Locate every leukocyte (white blood cell).
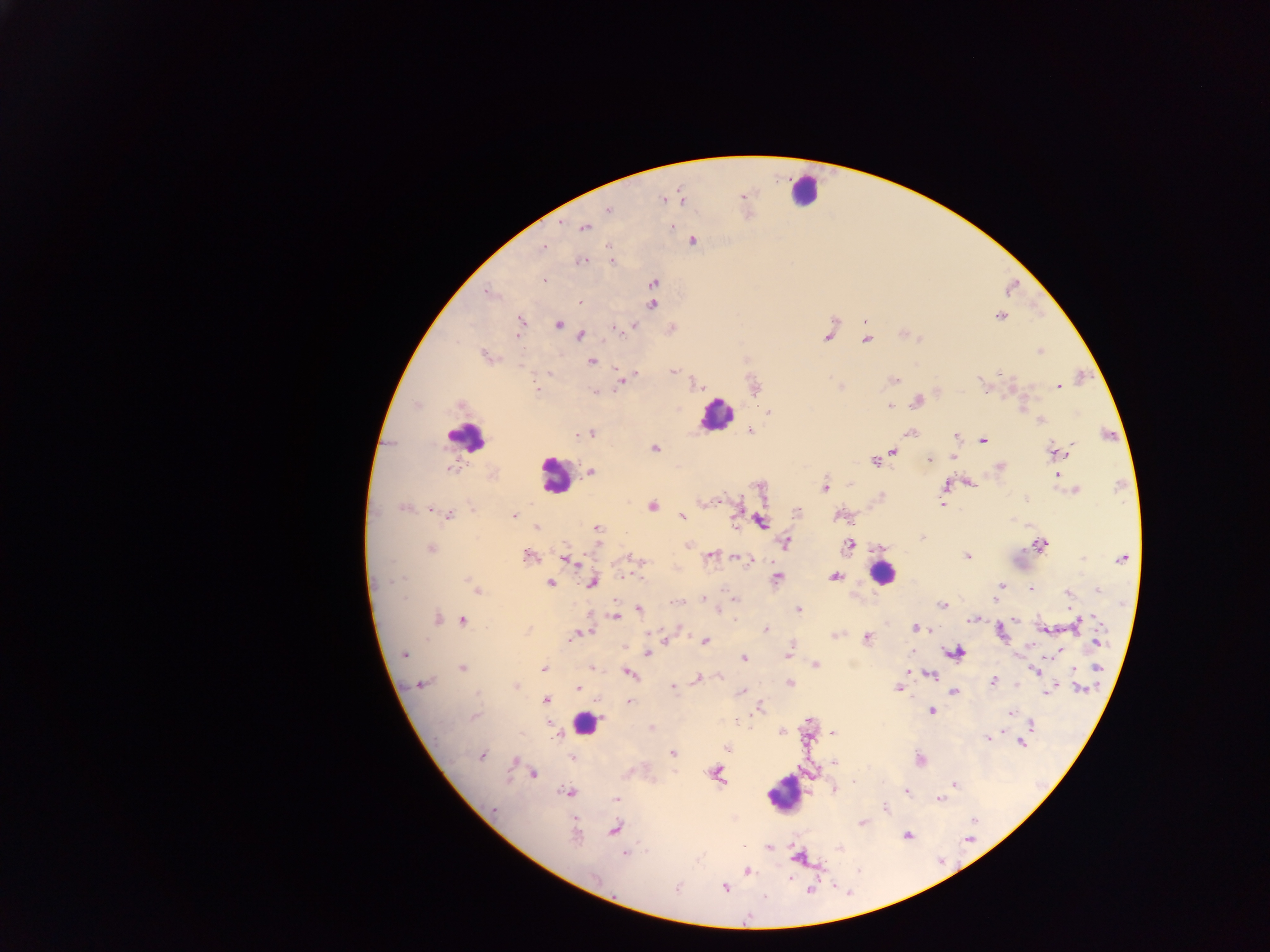
Approximate centers as x y in pixels.
Leukocytes: 805 189; 715 415; 465 438; 554 475; 881 574; 585 724; 786 791.

Plasmodium parasite locations = approximate centers as x y in pixels: 742 196; 663 200; 609 209; 672 227; 585 228; 693 241; 544 246; 582 260; 611 261; 543 280; 653 283; 488 293; 580 303; 652 305; 1000 316; 520 321; 559 325; 633 326; 614 327; 580 336; 828 337; 866 340; 1040 351; 485 355; 592 362; 673 371; 634 375; 623 379; 894 379; 981 382; 1058 387; 537 389; 756 389; 596 391; 917 401; 459 406; 889 406; 768 412; 1041 420; 750 431; 910 432; 591 434; 577 435; 955 437; 982 440; 654 449; 893 451; 1058 453; 929 460; 875 461; 999 467; 449 468; 590 471; 1057 474; 969 483; 946 485; 825 487; 1076 490; 881 496; 942 505; 652 506; 403 508; 434 511; 798 511; 448 515; 838 515; 514 516; 682 517; 761 521; 537 528; 597 529; 922 537; 785 543; 688 545; 849 545; 1040 545; 431 548; 528 556; 710 556; 967 557; 739 558; 566 559; 635 559; 1122 559; 748 561; 835 577; 778 578; 399 580; 470 582; 550 583; 593 583; 1001 585; 1030 588; 1099 589; 478 591; 997 593; 1069 593; 703 599; 735 599; 995 599; 677 602; 942 605; 799 609; 640 610; 615 616; 734 618; 437 619; 973 619; 1097 619; 1015 620; 463 621; 1077 623; 917 627; 765 629; 678 630; 577 634; 835 635; 571 637; 867 639; 704 642; 1098 642; 792 647; 789 652; 957 652; 647 653; 1056 653; 404 654; 744 658; 815 665; 462 667; 591 667; 543 668; 910 669; 1098 669; 1036 671; 630 674; 718 676; 931 676; 697 679; 992 681; 422 684; 790 684; 515 686; 673 687; 577 688; 898 688; 1081 689; 743 691; 954 691; 1047 691; 546 700; 630 701; 759 709; 931 710; 1011 713; 475 717; 1032 725; 782 731; 833 732; 987 738; 1021 744; 726 747; 672 753; 481 755; 572 757; 514 761; 834 762; 534 773; 717 774; 854 783; 954 785; 834 789; 567 792; 906 792; 616 799; 939 799; 885 808; 494 810; 862 823; 615 829; 907 835; 575 836; 768 847; 839 848; 625 854; 798 858; 748 871; 594 878; 677 888; 724 888; 811 890; 765 896
image size = 1270×952 pixels
country = Ghana
field of view = single
capture = mobile-phone photograph through a microscope
preparation = thick blood film